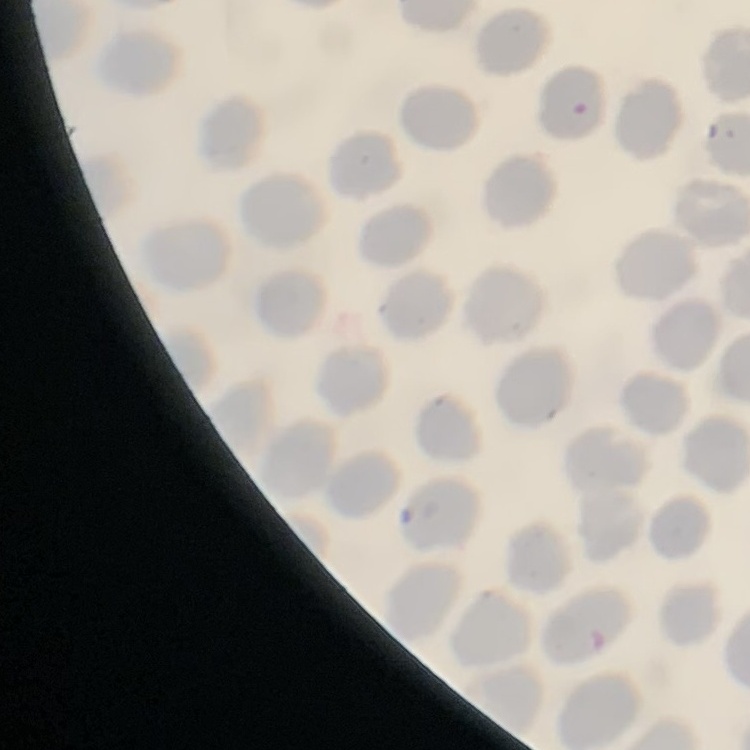
{
  "erythrocyte_morphology": "no rouleaux formation",
  "stain": "Field's or Giemsa",
  "preparation": "thin peripheral smear",
  "image_type": "one tile cut from a larger photomicrograph"
}